State which parasite is depicted.
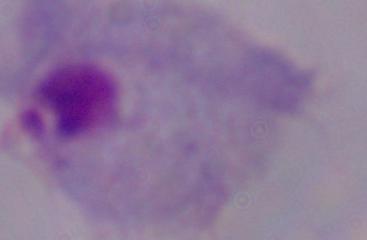

This is a trichomonad.

Micrograph. Captured at 1000x magnification.